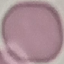
Result: negative for malaria parasites. Photographed with a smartphone camera at the microscope eyepiece. Automatically extracted cell patch, resized to 64 × 64 pixels. Thin smear of blood. Giemsa stain.